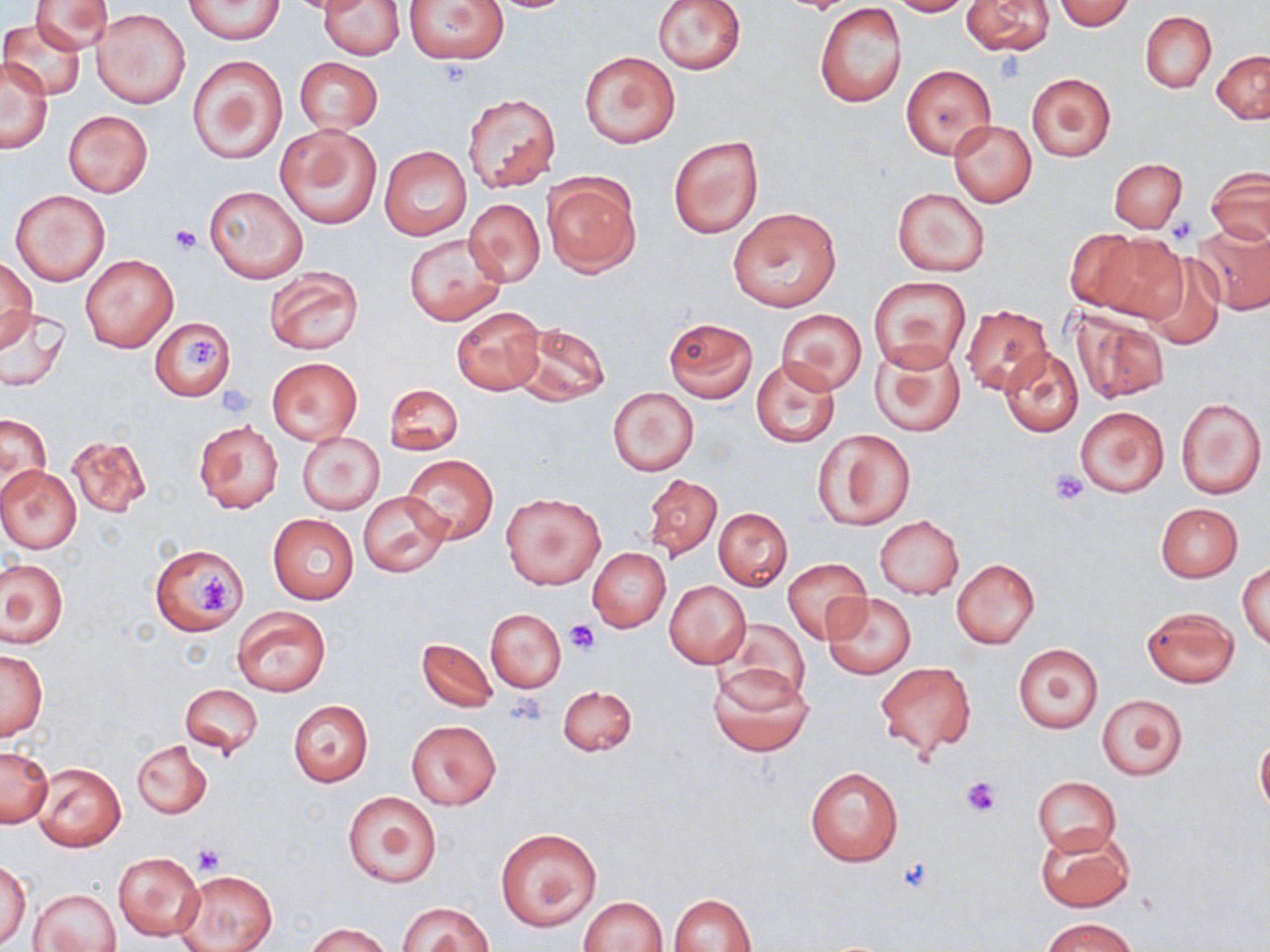

Approximate bounding boxes as (x1, y1, x2, y2) in pixels. Platelet locations: (995, 53, 1026, 84), (170, 226, 203, 255), (187, 338, 219, 372), (215, 384, 255, 418), (1050, 470, 1088, 505), (197, 572, 237, 616), (566, 619, 599, 653), (508, 694, 549, 728), (959, 776, 1001, 818), (192, 842, 225, 876), (895, 856, 938, 893). Uninfected red blood cell locations: (31, 0, 112, 55), (184, 0, 284, 44), (320, 0, 404, 60), (403, 0, 509, 64), (653, 0, 745, 74), (887, 0, 970, 16), (1054, 0, 1133, 30), (479, 1, 582, 13), (962, 1, 1054, 56), (814, 4, 907, 108), (91, 8, 190, 109), (1140, 11, 1215, 92), (2, 20, 85, 98), (1212, 50, 1270, 124), (580, 52, 680, 148), (189, 55, 287, 164), (294, 57, 383, 134), (1, 58, 53, 153), (901, 65, 994, 158), (1026, 72, 1115, 161), (462, 93, 560, 192), (64, 110, 152, 197), (949, 120, 1037, 206), (276, 124, 382, 229), (669, 136, 763, 239), (380, 145, 471, 241), (1110, 157, 1187, 233), (1206, 167, 1270, 245), (542, 174, 641, 275), (203, 185, 309, 283), (893, 188, 990, 276), (10, 190, 110, 285), (465, 198, 545, 287), (729, 207, 843, 312), (1192, 223, 1270, 314), (1064, 229, 1148, 311), (403, 232, 507, 325), (1086, 233, 1189, 325), (1137, 253, 1225, 349), (81, 255, 177, 352), (1, 258, 37, 346), (264, 266, 363, 356), (868, 275, 971, 372), (960, 305, 1053, 394), (1, 306, 71, 391), (451, 307, 545, 395), (1068, 307, 1170, 403), (775, 308, 867, 395), (150, 317, 235, 400), (663, 317, 758, 402), (513, 321, 610, 406), (870, 341, 966, 437), (1000, 346, 1084, 437), (266, 357, 362, 446), (751, 357, 841, 450), (384, 383, 464, 454), (608, 387, 698, 476), (1175, 396, 1266, 498), (1074, 404, 1170, 498), (2, 414, 53, 499), (194, 420, 284, 515), (813, 429, 915, 530), (297, 432, 384, 512), (67, 435, 151, 517), (401, 454, 498, 546), (0, 465, 82, 554), (641, 473, 722, 560), (357, 491, 450, 577), (501, 492, 605, 589), (1154, 503, 1243, 581), (713, 507, 792, 590), (268, 515, 359, 604), (875, 516, 964, 598), (150, 545, 247, 635), (587, 548, 670, 632), (784, 558, 870, 643), (951, 558, 1040, 647), (1, 559, 67, 647), (1238, 563, 1269, 649), (664, 580, 751, 669), (824, 592, 916, 678), (233, 607, 330, 696), (1142, 607, 1239, 688), (486, 609, 565, 693), (717, 617, 811, 705), (417, 637, 497, 712), (1013, 643, 1103, 733), (0, 647, 48, 741), (875, 661, 977, 760), (707, 665, 814, 758), (178, 683, 262, 757), (559, 685, 636, 756), (1096, 692, 1187, 781), (288, 700, 374, 786), (406, 718, 502, 811), (1256, 735, 1270, 817), (132, 740, 212, 818), (0, 746, 53, 827), (34, 763, 126, 852), (804, 766, 904, 867), (1033, 776, 1121, 854), (340, 790, 441, 887), (1035, 825, 1136, 913), (495, 827, 602, 932), (114, 851, 205, 942), (0, 861, 31, 946), (175, 870, 278, 952), (32, 889, 121, 952), (671, 893, 756, 952), (580, 896, 667, 951), (397, 902, 494, 952), (1042, 917, 1135, 952), (307, 922, 390, 952). Slide-level diagnosis: negative for blood parasites. Optical microscopy. Captured at 1000x magnification. Image is 1270×952 pixels. May-Grünwald-Giemsa-stained preparation. Single field of view. Thin blood smear.